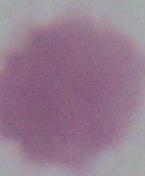
Micrograph. An erythrocyte is seen. Captured at 1000x magnification.